State which parasite is depicted.
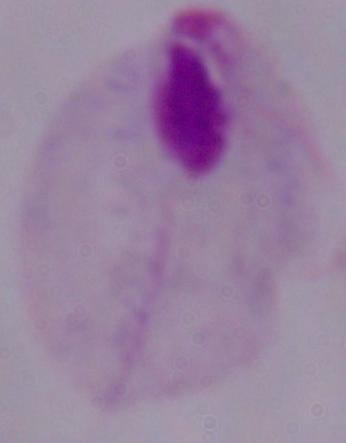

A trichomonad.

Summary:
  - Modality: photomicrograph
  - Magnification: 1000x